Assess the morphology of the red blood cells.
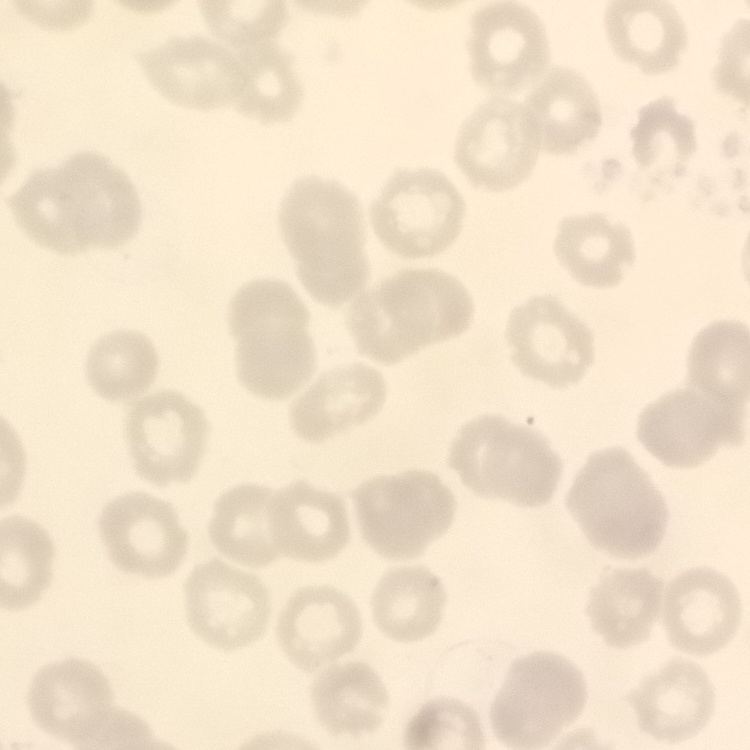

They show no rouleaux formation.

Thin blood smear. Field's or Giemsa stain. Square crop of a larger photomicrograph.